State which parasite is depicted.
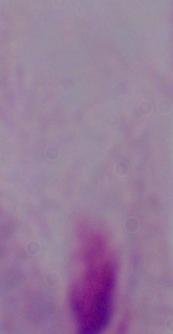

A trichomonad.

magnification = 1000x
modality = micrograph